Classify this cell by malaria status.
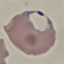
It is parasitized.

Giemsa-stained preparation. Thin blood smear. Photographed with a smartphone camera at the microscope eyepiece. Cell patch, automatically extracted from a larger field of view and resized to 64 × 64 pixels.